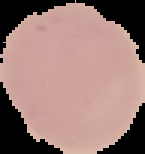

Result: no malaria parasites detected. The area outside the segmented cell region is set to black. Image is 145×154 pixels. From a thin blood smear.